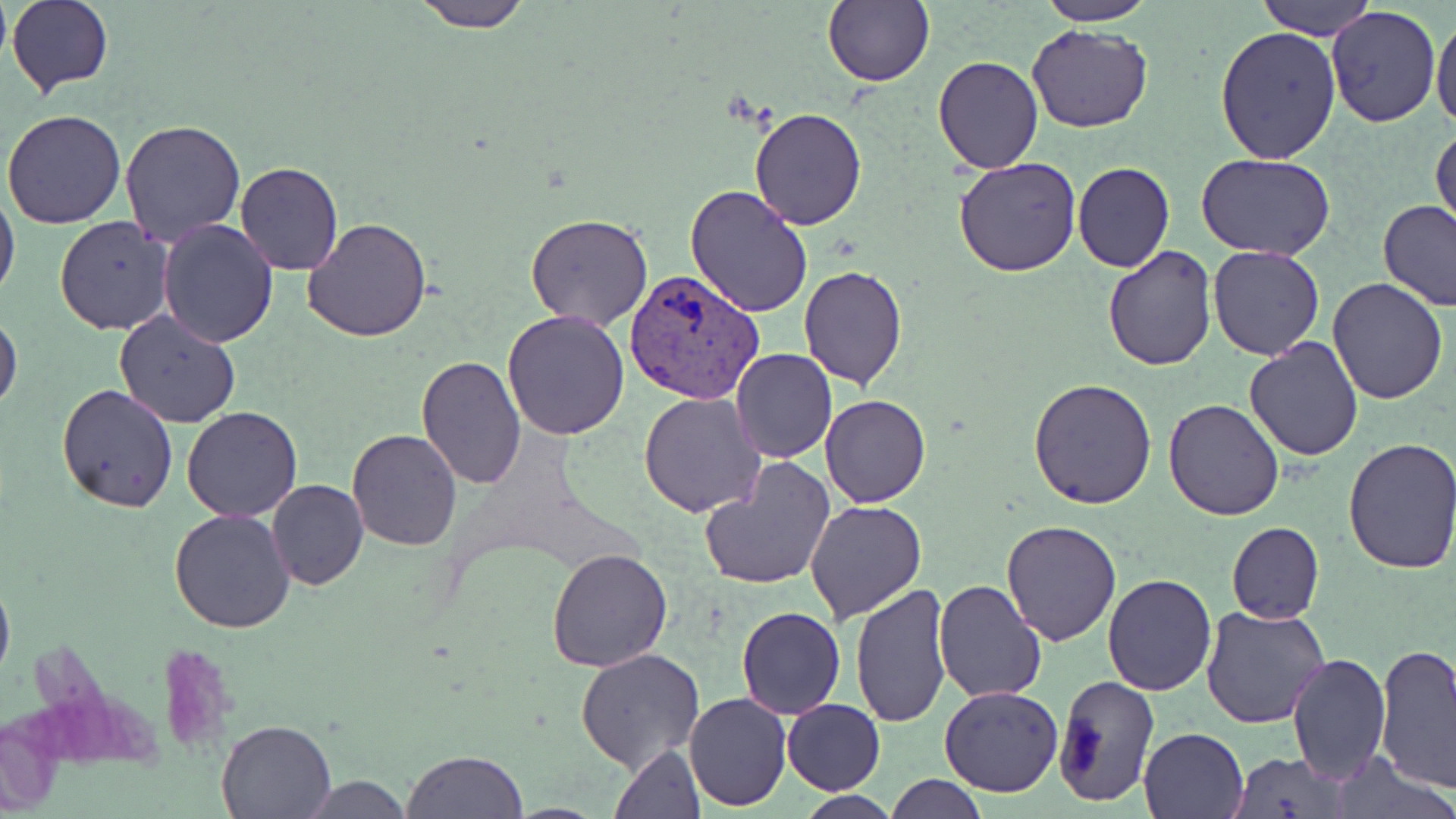

slide-level diagnosis = Plasmodium vivax
modality = light microscopy
image size = 1456×819 pixels
stain = May-Grünwald-Giemsa
field of view = one of a larger specimen
magnification = 1000x
preparation = thin blood smear
uninfected red blood cell locations = approximate bounding boxes as [x1, y1, x2, y2] in pixels: [8, 0, 112, 95], [825, 0, 933, 86], [1037, 0, 1156, 25], [1259, 0, 1379, 39], [411, 1, 530, 31], [1327, 5, 1440, 127], [1431, 14, 1456, 132], [1026, 24, 1151, 133], [1215, 25, 1342, 164], [933, 54, 1043, 173], [748, 105, 867, 229], [3, 107, 128, 229], [119, 119, 248, 247], [1431, 125, 1455, 237], [1195, 152, 1337, 259], [953, 156, 1082, 277], [1073, 161, 1175, 273], [234, 162, 343, 276], [686, 183, 814, 318], [0, 191, 20, 300], [1376, 198, 1456, 311], [525, 212, 654, 331], [55, 215, 174, 335], [304, 216, 432, 342], [157, 220, 279, 348], [1103, 244, 1216, 371], [1208, 246, 1325, 362], [798, 265, 907, 391], [1327, 280, 1448, 405], [502, 309, 629, 440], [113, 310, 241, 429], [0, 313, 22, 411], [1244, 336, 1364, 461], [731, 348, 839, 463], [417, 353, 524, 489], [1027, 377, 1158, 508], [57, 385, 179, 514], [639, 392, 766, 517], [821, 393, 931, 508], [1163, 397, 1287, 521], [182, 405, 303, 523], [348, 427, 461, 549], [1340, 437, 1456, 578], [700, 458, 834, 592], [266, 477, 368, 591], [805, 501, 927, 622], [170, 508, 295, 632], [1001, 519, 1122, 644], [1225, 522, 1324, 624], [546, 548, 674, 670], [0, 572, 14, 686], [1103, 574, 1216, 694], [932, 579, 1047, 701], [849, 582, 953, 727], [736, 605, 845, 719], [1200, 606, 1330, 730], [1375, 644, 1456, 794], [576, 648, 706, 774], [1286, 651, 1390, 782], [1054, 675, 1161, 806], [939, 685, 1066, 797], [684, 692, 791, 810], [781, 698, 885, 794], [216, 719, 338, 816], [1138, 726, 1250, 819], [610, 743, 706, 819], [403, 749, 528, 818], [1231, 751, 1346, 816], [1333, 755, 1455, 818], [884, 774, 988, 818], [298, 776, 416, 817], [793, 792, 901, 819]
Plasmodium vivax-infected red blood cell locations = approximate bounding boxes as [x1, y1, x2, y2] in pixels: [623, 266, 764, 403]